Identify the parasite.
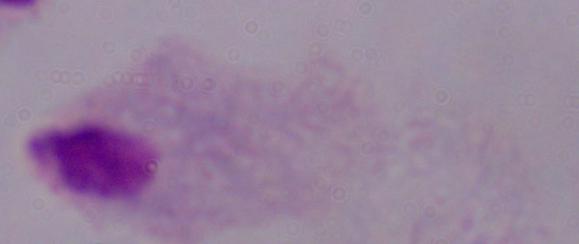

A trichomonad.

Photomicrograph. Captured at 1000x magnification.